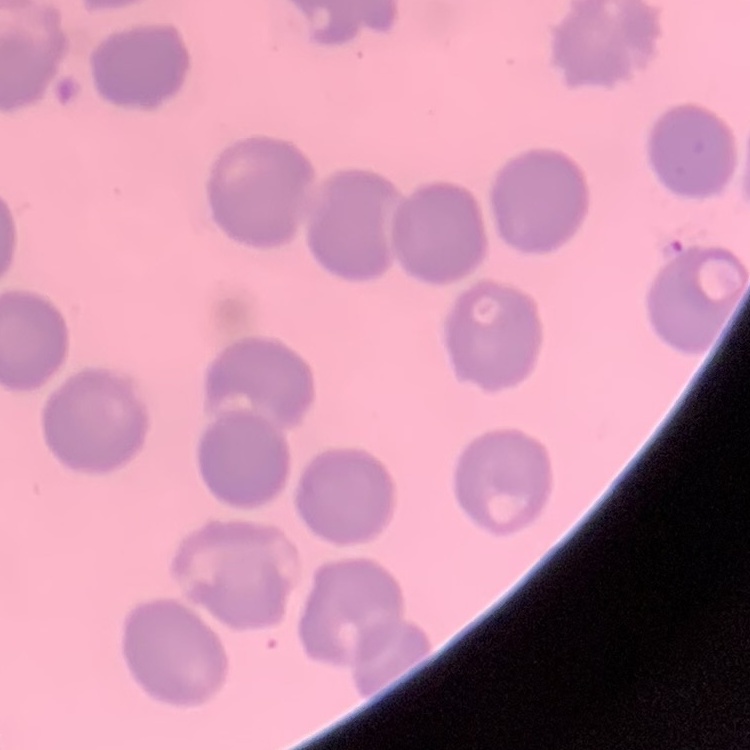

Summary:
  - Red blood cell morphology: no rouleaux formation
  - Image type: one tile cut from a larger photomicrograph
  - Stain: Field's or Giemsa
  - Preparation: thin blood smear